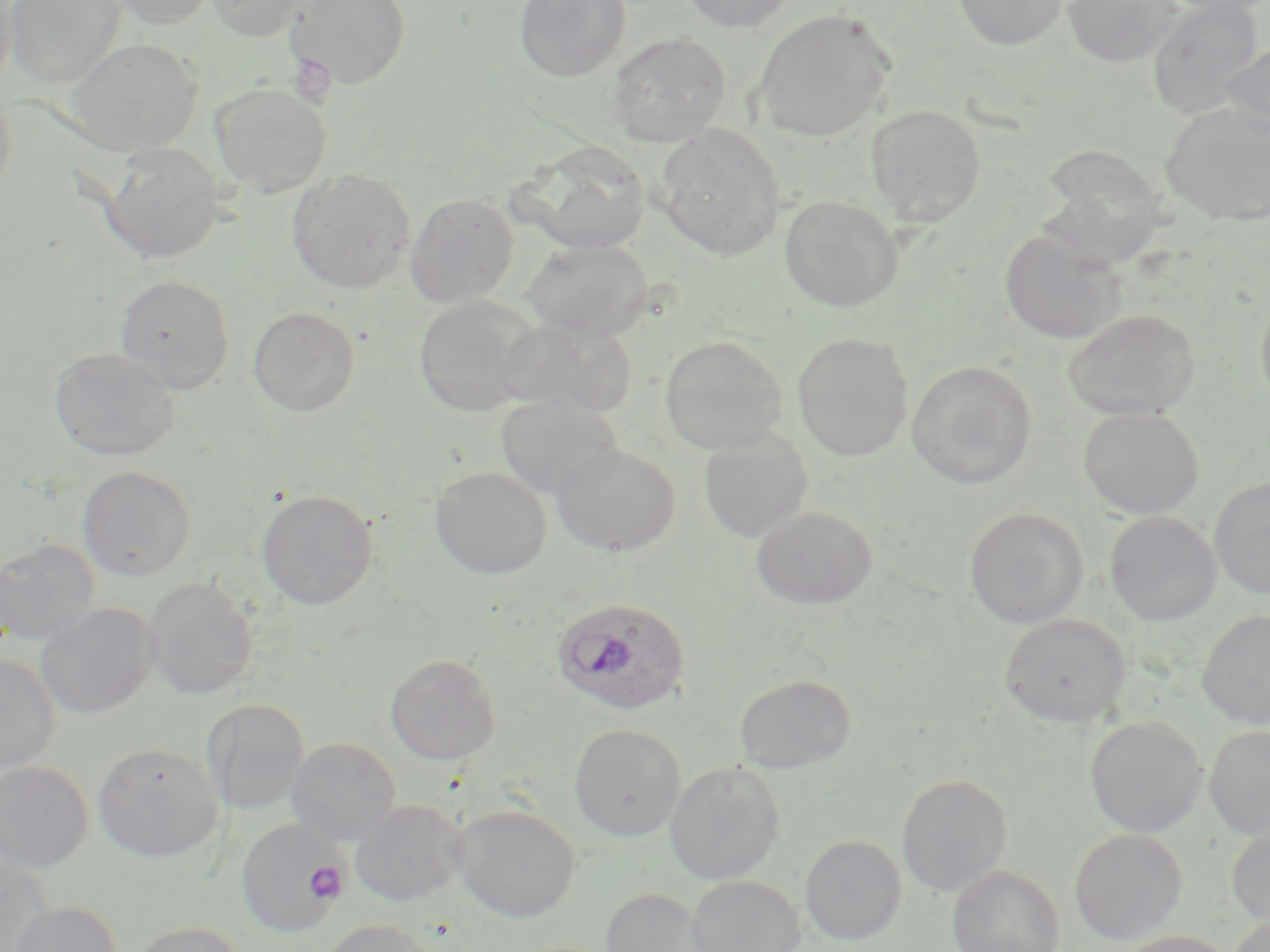

slide-level diagnosis = Plasmodium ovale
image size = 1270×952 pixels
uninfected red blood cell locations = approximate bounding boxes as (x1, y1, x2, y2) in pixels: (0, 0, 17, 90), (4, 0, 125, 89), (109, 0, 219, 29), (206, 0, 316, 41), (285, 0, 411, 90), (514, 0, 631, 82), (682, 0, 797, 33), (953, 0, 1066, 50), (1061, 0, 1184, 66), (1146, 0, 1266, 119), (1157, 0, 1270, 17), (751, 9, 895, 142), (606, 32, 732, 148), (65, 38, 203, 154), (1221, 41, 1270, 139), (0, 81, 17, 200), (210, 82, 332, 197), (1160, 102, 1270, 225), (864, 104, 986, 225), (654, 125, 786, 260), (99, 142, 224, 263), (521, 142, 651, 254), (1036, 144, 1172, 263), (286, 168, 416, 294), (404, 192, 519, 307), (779, 195, 904, 312), (999, 229, 1126, 344), (523, 239, 654, 342), (114, 275, 235, 393), (1255, 290, 1270, 415), (413, 295, 540, 416), (247, 307, 360, 416), (1062, 308, 1200, 420), (497, 317, 638, 418), (792, 333, 913, 461), (659, 334, 788, 453), (48, 346, 180, 460), (906, 360, 1038, 489), (495, 395, 623, 501), (1078, 407, 1204, 518), (698, 428, 813, 541), (550, 444, 680, 556), (77, 466, 196, 581), (430, 467, 552, 578), (1209, 477, 1270, 598), (256, 489, 378, 609), (751, 506, 878, 609), (964, 507, 1088, 627), (1105, 511, 1221, 625), (0, 538, 100, 645), (142, 577, 258, 700), (35, 603, 158, 719), (1197, 610, 1270, 728), (999, 614, 1130, 727), (385, 654, 502, 765), (0, 655, 61, 774), (734, 674, 856, 772), (201, 699, 310, 814), (1085, 716, 1206, 837), (569, 723, 685, 840), (1203, 724, 1270, 839), (286, 737, 402, 846), (92, 742, 223, 862), (0, 760, 93, 872), (665, 761, 784, 885), (896, 773, 1012, 896), (351, 800, 467, 906), (451, 803, 580, 922), (237, 818, 346, 939), (1227, 823, 1270, 928), (1069, 829, 1187, 944), (800, 835, 906, 945), (0, 851, 56, 952), (948, 866, 1064, 952), (685, 876, 805, 952), (600, 887, 714, 952), (9, 901, 123, 952), (1229, 916, 1270, 952), (317, 919, 441, 952), (129, 921, 249, 952), (1112, 931, 1242, 952)
field of view = one of a larger specimen
magnification = 1000x
Plasmodium ovale-infected red blood cell locations = approximate bounding boxes as (x1, y1, x2, y2) in pixels: (550, 596, 693, 717)
modality = light microscopy
platelet locations = approximate bounding boxes as (x1, y1, x2, y2) in pixels: (287, 53, 336, 105), (304, 860, 348, 903)
stain = May-Grünwald-Giemsa
preparation = thin blood film